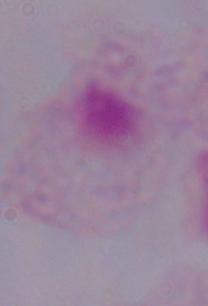 A trichomonad is seen. 1000x magnification. Micrograph.